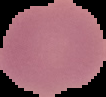
From a thin blood smear. Result: negative for Plasmodium parasites. Segmented cell region on a black background. Image is 106×97 pixels.